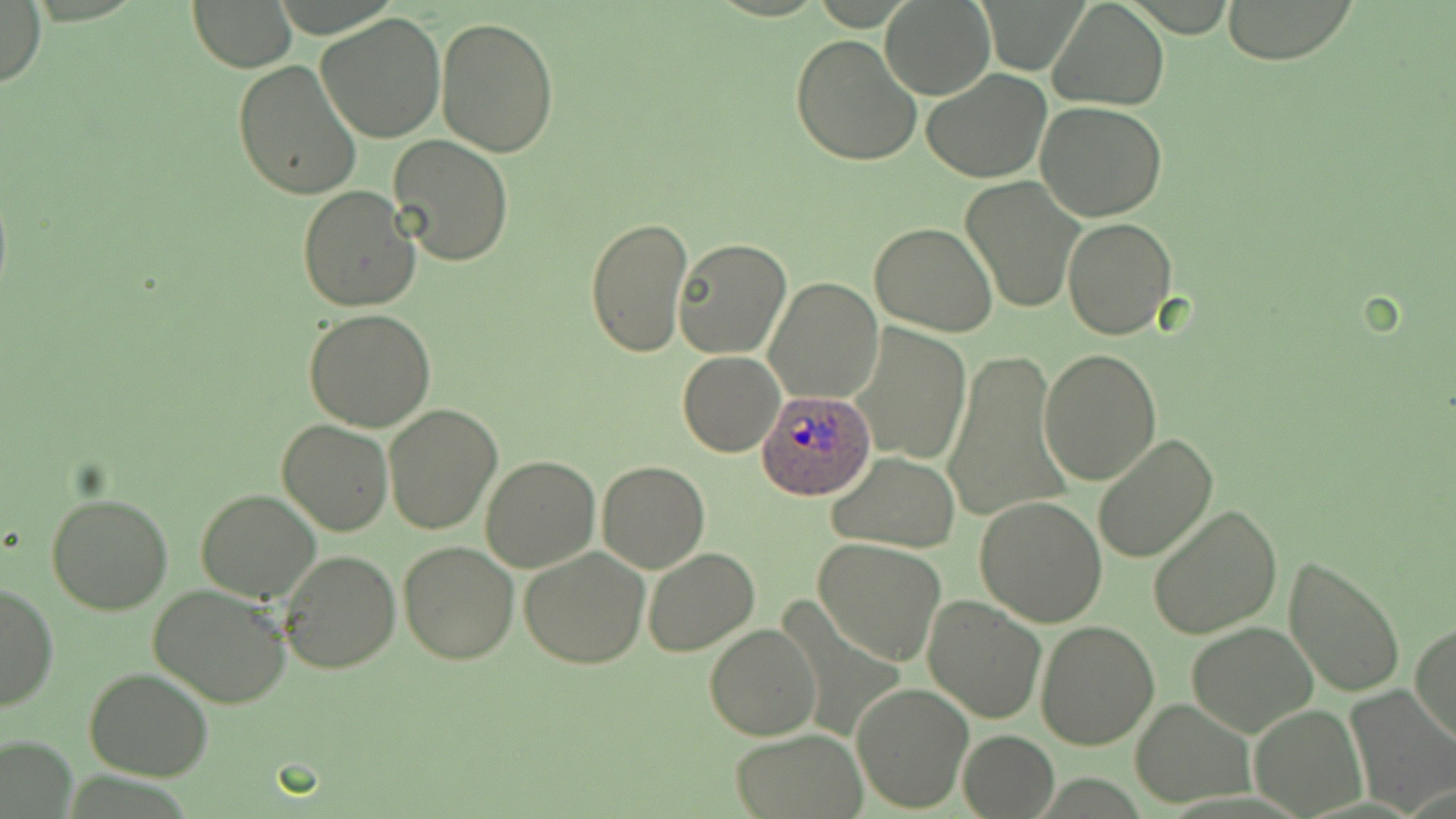

slide_level_diagnosis: Plasmodium ovale
image_size: 1456×819 pixels
preparation: thin blood film
field_of_view: one of a larger specimen
magnification: 1000x
uninfected_red_blood_cell_locations: 'approximate bounding boxes as (x1,y1)-(x2,y2) corner pairs in pixels: (1220,0)-(1356,64), (1,1)-(46,91), (881,1)-(993,100), (189,2)-(296,72), (1051,4)-(1169,112), (316,11)-(448,141), (436,18)-(559,158), (790,34)-(924,167), (233,60)-(362,199), (921,68)-(1053,184), (1036,100)-(1168,221), (387,133)-(512,267), (959,177)-(1084,313), (297,185)-(422,313), (1061,215)-(1178,339), (585,216)-(695,360), (868,220)-(998,336), (672,238)-(792,360), (765,277)-(883,405), (304,307)-(437,431), (849,322)-(972,466), (942,347)-(1072,526), (1038,349)-(1161,485), (678,351)-(785,457), (383,404)-(503,535), (278,418)-(393,536), (1090,433)-(1218,564), (828,452)-(961,552), (479,453)-(600,573), (597,461)-(712,573), (196,489)-(322,603), (47,491)-(173,614), (976,494)-(1109,628), (1147,503)-(1282,639), (814,539)-(946,665), (398,540)-(521,664), (518,546)-(650,669), (641,546)-(759,657), (277,551)-(401,674), (1281,554)-(1405,700), (0,582)-(57,713), (147,584)-(290,708), (922,593)-(1047,724), (1187,620)-(1317,736), (1036,621)-(1159,751), (1410,621)-(1455,751), (704,623)-(822,741), (84,667)-(213,780), (851,681)-(974,813), (1344,688)-(1455,815), (1130,696)-(1254,806), (1249,702)-(1366,816), (956,729)-(1058,817), (727,730)-(867,818), (2,736)-(74,816)'
modality: optical microscopy
plasmodium_ovale_infected_red_blood_cell_locations: 'approximate bounding boxes as (x1,y1)-(x2,y2) corner pairs in pixels: (756,386)-(877,503)'
stain: May-Grünwald-Giemsa